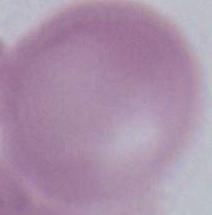
{
  "magnification": "1000x",
  "identification": "red blood cell",
  "modality": "photomicrograph"
}